Mark where platelets are.
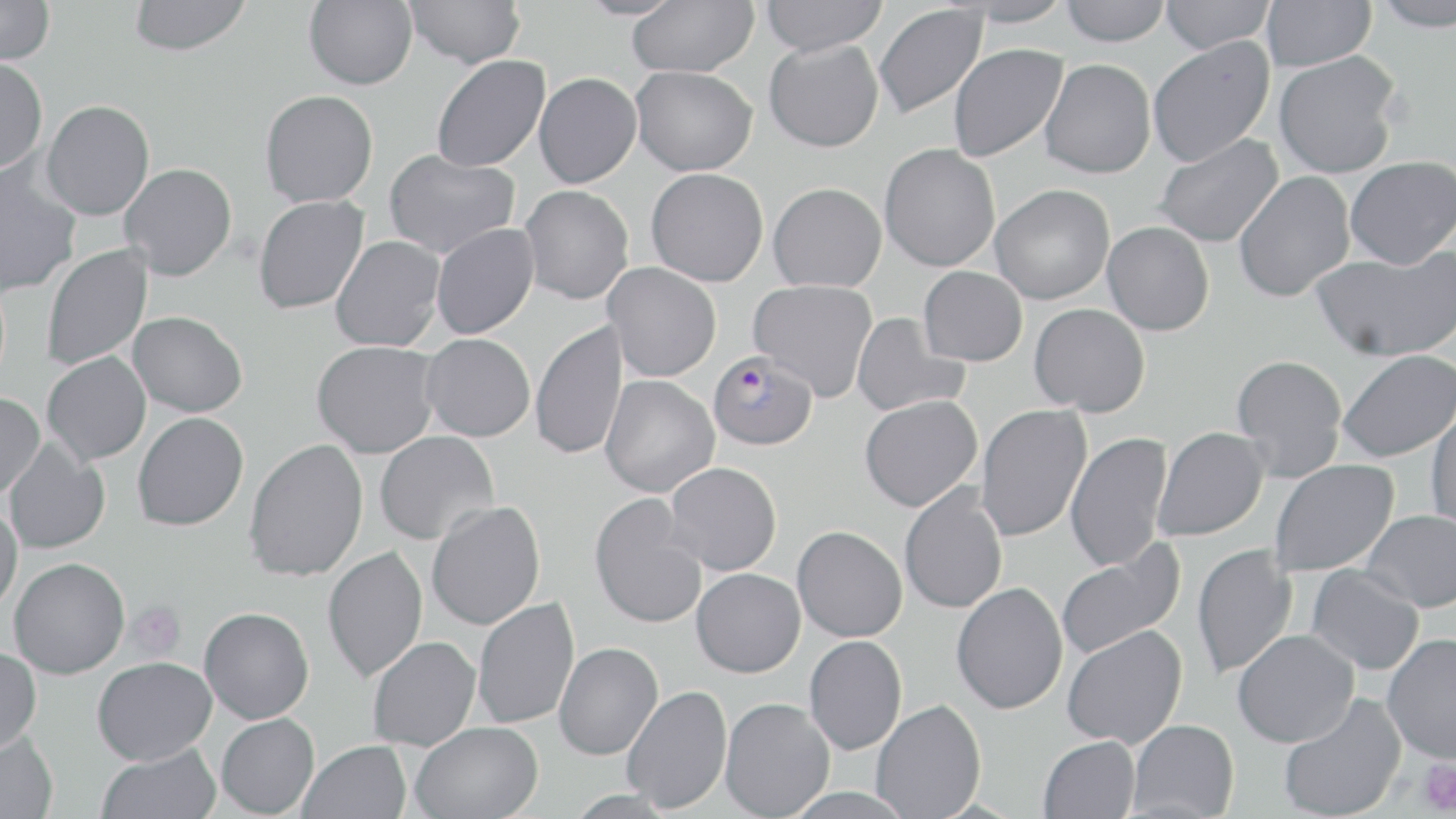
Approximate bounding boxes as (x1, y1, x2, y2) in pixels.
Platelets: (125, 601, 186, 661), (1416, 757, 1456, 816).

Summary:
  - Plasmodium falciparum-infected red blood cell locations: (707, 350, 818, 450)
  - Uninfected red blood cell locations: (0, 0, 55, 66), (128, 0, 252, 56), (304, 0, 417, 90), (405, 0, 525, 68), (627, 0, 758, 77), (760, 0, 889, 56), (957, 0, 1075, 27), (1058, 0, 1171, 46), (1159, 0, 1274, 53), (1261, 0, 1376, 71), (1371, 1, 1456, 32), (873, 4, 988, 120), (1147, 37, 1275, 166), (764, 38, 884, 152), (948, 43, 1068, 162), (1273, 52, 1402, 179), (431, 55, 550, 172), (0, 58, 48, 174), (1039, 59, 1156, 179), (630, 65, 757, 176), (533, 72, 642, 188), (260, 90, 378, 207), (41, 100, 155, 220), (1153, 133, 1285, 248), (879, 143, 1001, 272), (383, 150, 520, 259), (1344, 156, 1456, 269), (0, 163, 81, 297), (119, 163, 237, 281), (646, 167, 769, 287), (1233, 171, 1355, 302), (768, 182, 886, 292), (990, 184, 1115, 304), (520, 185, 634, 305), (253, 195, 369, 314), (1103, 221, 1215, 335), (431, 224, 539, 339), (331, 236, 445, 351), (40, 243, 153, 371), (1310, 247, 1456, 361), (603, 262, 721, 381), (918, 266, 1028, 366), (748, 279, 878, 401), (1028, 303, 1150, 417), (128, 311, 248, 417), (852, 313, 968, 417), (530, 319, 628, 461), (421, 333, 535, 442), (311, 341, 440, 459), (1336, 349, 1456, 463), (41, 351, 151, 465), (1230, 354, 1348, 481), (600, 376, 720, 498), (0, 392, 45, 499), (859, 395, 982, 512), (976, 404, 1092, 542), (1425, 405, 1456, 530), (132, 412, 248, 531), (1152, 427, 1269, 541), (374, 431, 500, 546), (1065, 431, 1172, 573), (3, 437, 110, 554), (243, 438, 368, 582), (1269, 459, 1399, 577), (665, 461, 782, 575), (899, 483, 1008, 614), (588, 494, 707, 630), (426, 501, 546, 630), (0, 505, 23, 613), (1360, 510, 1456, 612), (792, 526, 907, 642), (1055, 543, 1186, 661), (322, 544, 428, 683), (1192, 544, 1297, 679), (8, 557, 130, 678), (1306, 565, 1425, 675), (691, 568, 805, 678), (951, 582, 1068, 714), (472, 597, 579, 729), (199, 606, 314, 723), (1062, 624, 1187, 749), (1232, 629, 1359, 747), (1381, 632, 1456, 764), (804, 635, 907, 754), (367, 636, 481, 751), (554, 642, 663, 760), (0, 646, 42, 754), (91, 657, 217, 765), (622, 684, 732, 814), (1277, 692, 1407, 819), (720, 697, 835, 819), (870, 699, 986, 819), (216, 713, 320, 817), (1128, 719, 1239, 818), (410, 721, 543, 819), (0, 730, 58, 819), (1038, 735, 1141, 819), (298, 740, 411, 819), (95, 744, 221, 819)
  - Slide-level diagnosis: Plasmodium falciparum
  - Preparation: thin blood smear
  - Stain: May-Grünwald-Giemsa
  - Image size: 1456×819 pixels
  - Magnification: 1000x
  - Modality: light microscopy
  - Field of view: one of a larger specimen